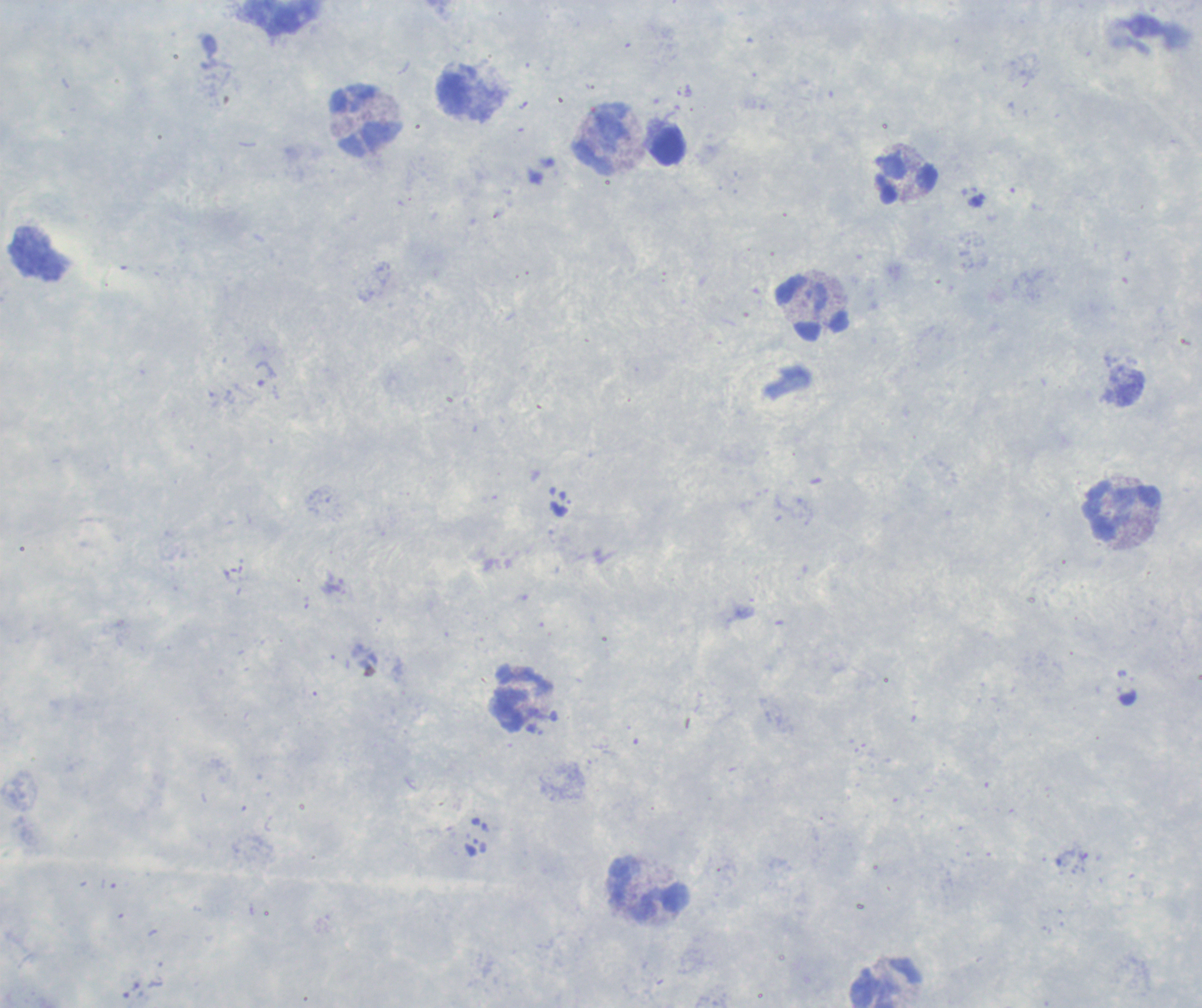 Approximate object centers, in pixels from the top-left corner. Trophozoite locations: (x=264, y=373). Leukocyte locations: (x=281, y=17), (x=364, y=121), (x=604, y=140), (x=669, y=146), (x=907, y=179), (x=813, y=309), (x=1122, y=512), (x=521, y=697), (x=649, y=890), (x=886, y=983). Coloration quality: good. Image is 1202×1008 pixels. Captured at 100x magnification. Previously used in an actual diagnosis. Single field of view. Romanowsky stain. Background quality: poor. Thick smear of blood. Result: positive for Plasmodium parasites.